Assess the morphology of the erythrocytes.
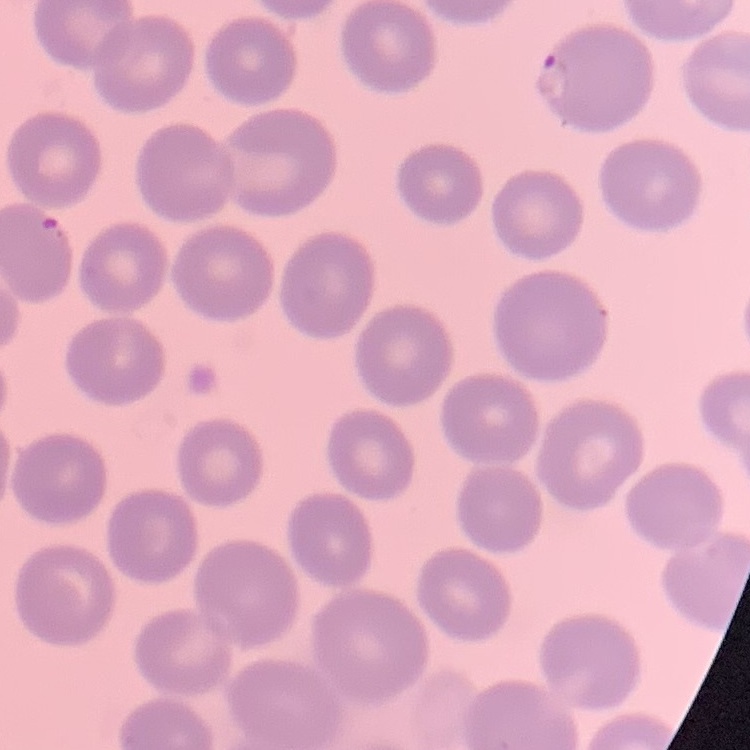

No rouleaux formation.

Square crop of a larger photomicrograph. Thin blood smear. Field's or Giemsa stain.